Assess this cell for malaria.
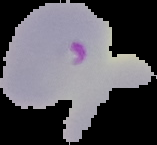

It is parasitized.

From a thin blood smear. The area outside the segmented cell region is set to black. Image is 157×145 pixels.